Assess this cell for malaria.
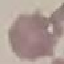

Uninfected.

stain: Giemsa
capture: smartphone camera at the microscope eyepiece
image_type: cell patch, automatically extracted from a larger field of view and resized to 64 × 64 pixels
preparation: thin blood smear